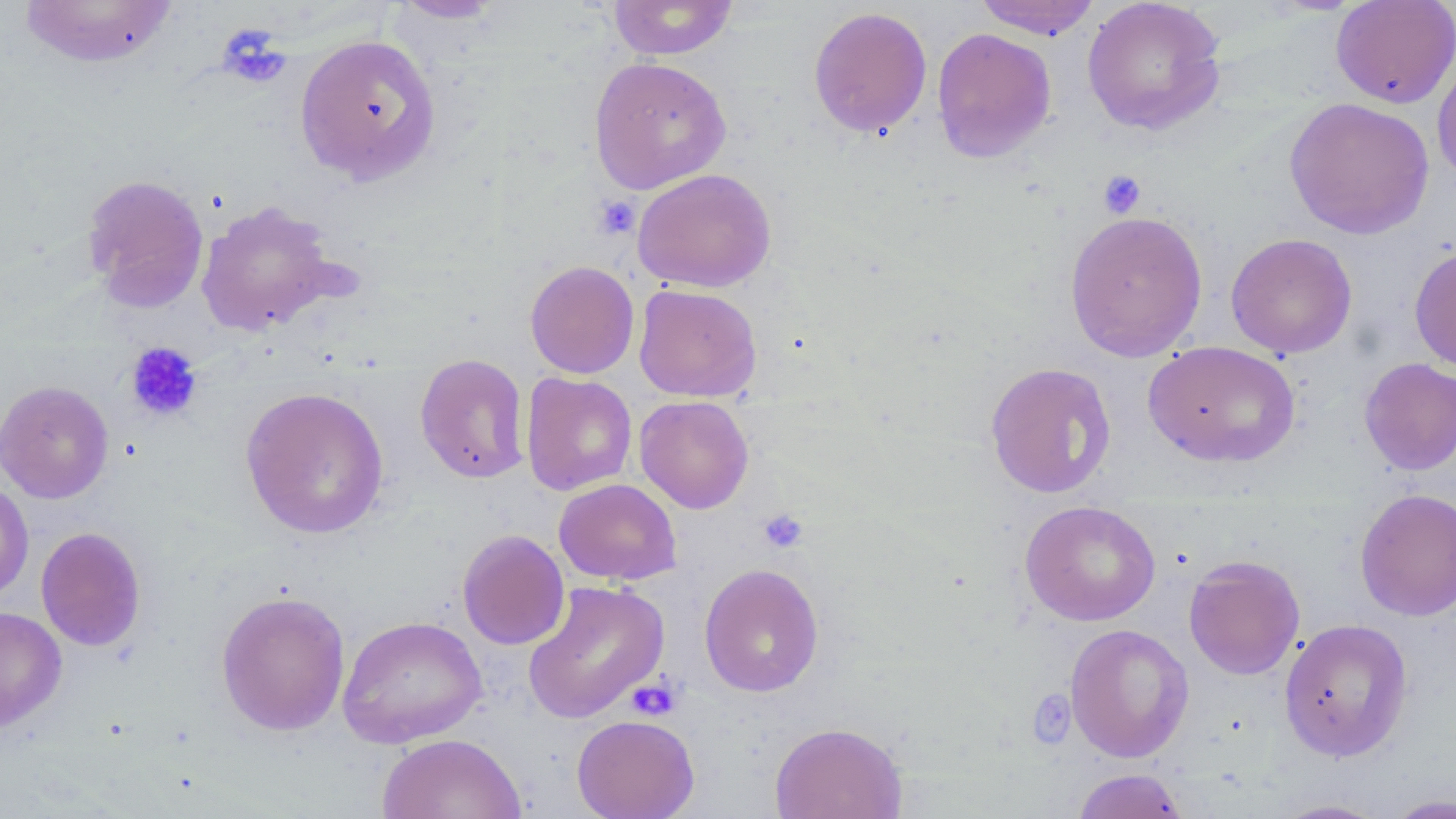

Approximate bounding boxes as named x1/y1/x2/y2 corners in pixels. Platelet locations: (x1=217, y1=23, x2=291, y2=89), (x1=1098, y1=170, x2=1147, y2=218), (x1=592, y1=195, x2=641, y2=241), (x1=125, y1=341, x2=203, y2=423), (x1=757, y1=508, x2=809, y2=554), (x1=626, y1=677, x2=682, y2=722), (x1=1027, y1=689, x2=1077, y2=748). Uninfected red blood cell locations: (x1=388, y1=0, x2=510, y2=24), (x1=973, y1=0, x2=1102, y2=39), (x1=1081, y1=0, x2=1227, y2=137), (x1=1330, y1=0, x2=1456, y2=108), (x1=16, y1=1, x2=180, y2=69), (x1=607, y1=1, x2=738, y2=60), (x1=808, y1=6, x2=932, y2=138), (x1=931, y1=27, x2=1057, y2=163), (x1=295, y1=33, x2=441, y2=185), (x1=1433, y1=51, x2=1456, y2=185), (x1=588, y1=55, x2=732, y2=194), (x1=1284, y1=97, x2=1434, y2=239), (x1=631, y1=168, x2=776, y2=292), (x1=81, y1=173, x2=210, y2=312), (x1=196, y1=200, x2=343, y2=336), (x1=1064, y1=210, x2=1208, y2=362), (x1=1225, y1=232, x2=1357, y2=359), (x1=1409, y1=244, x2=1456, y2=373), (x1=525, y1=260, x2=639, y2=379), (x1=633, y1=283, x2=762, y2=402), (x1=1143, y1=341, x2=1301, y2=467), (x1=415, y1=353, x2=530, y2=483), (x1=1359, y1=358, x2=1456, y2=475), (x1=984, y1=362, x2=1117, y2=498), (x1=521, y1=373, x2=637, y2=496), (x1=0, y1=379, x2=114, y2=504), (x1=240, y1=386, x2=390, y2=539), (x1=634, y1=395, x2=755, y2=514), (x1=0, y1=476, x2=34, y2=605), (x1=554, y1=478, x2=681, y2=585), (x1=1354, y1=488, x2=1456, y2=621), (x1=1020, y1=500, x2=1160, y2=626), (x1=35, y1=526, x2=147, y2=652), (x1=457, y1=529, x2=570, y2=650), (x1=1183, y1=554, x2=1306, y2=680), (x1=699, y1=563, x2=824, y2=697), (x1=522, y1=579, x2=670, y2=724), (x1=215, y1=589, x2=351, y2=736), (x1=0, y1=606, x2=67, y2=733), (x1=337, y1=615, x2=487, y2=748), (x1=1278, y1=617, x2=1414, y2=762), (x1=1064, y1=623, x2=1194, y2=762), (x1=571, y1=714, x2=699, y2=819), (x1=769, y1=721, x2=908, y2=819), (x1=377, y1=733, x2=527, y2=819), (x1=1073, y1=768, x2=1187, y2=818), (x1=1383, y1=793, x2=1456, y2=818), (x1=1268, y1=797, x2=1391, y2=818). Slide-level diagnosis: negative for blood parasites. May-Grünwald-Giemsa-stained preparation. One field of a larger specimen. 1000x magnification. Optical microscopy. Thin blood film. Image is 1456×819 pixels.